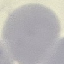
Summary:
  - Result: no malaria parasites seen
  - Preparation: thin blood smear
  - Stain: Giemsa
  - Capture: smartphone through the microscope eyepiece
  - Image type: cell patch, automatically extracted from a larger field of view and resized to 64 × 64 pixels